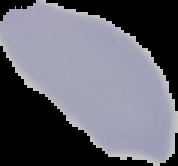
Summary:
  - Image type: segmented cell region on a black background
  - Preparation: thin blood film
  - Image size: 178×166 pixels
  - Result: no malaria parasites detected